Assess the morphology of the erythrocytes.
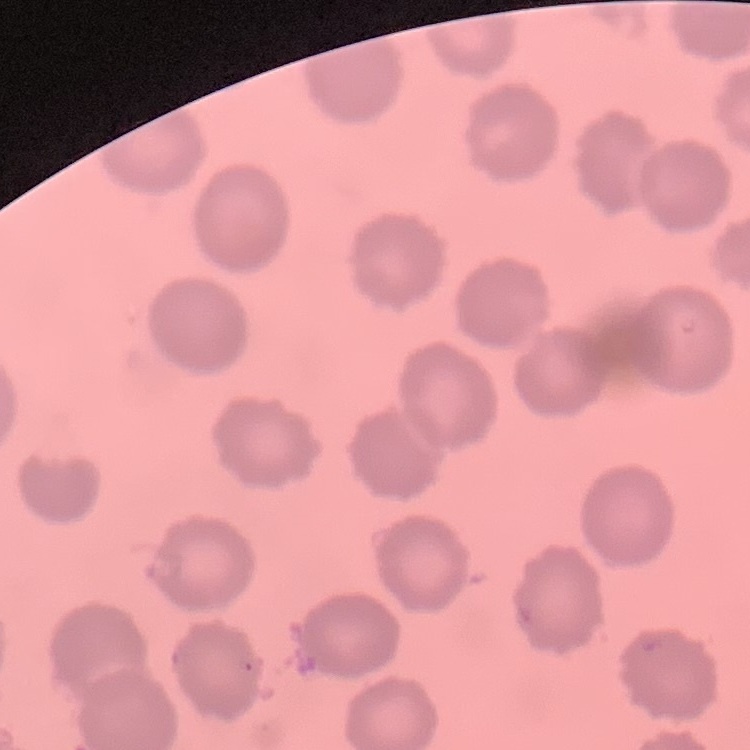

No rouleaux formation.

Field's or Giemsa stain. One tile cut from a larger photomicrograph. Thin blood smear.